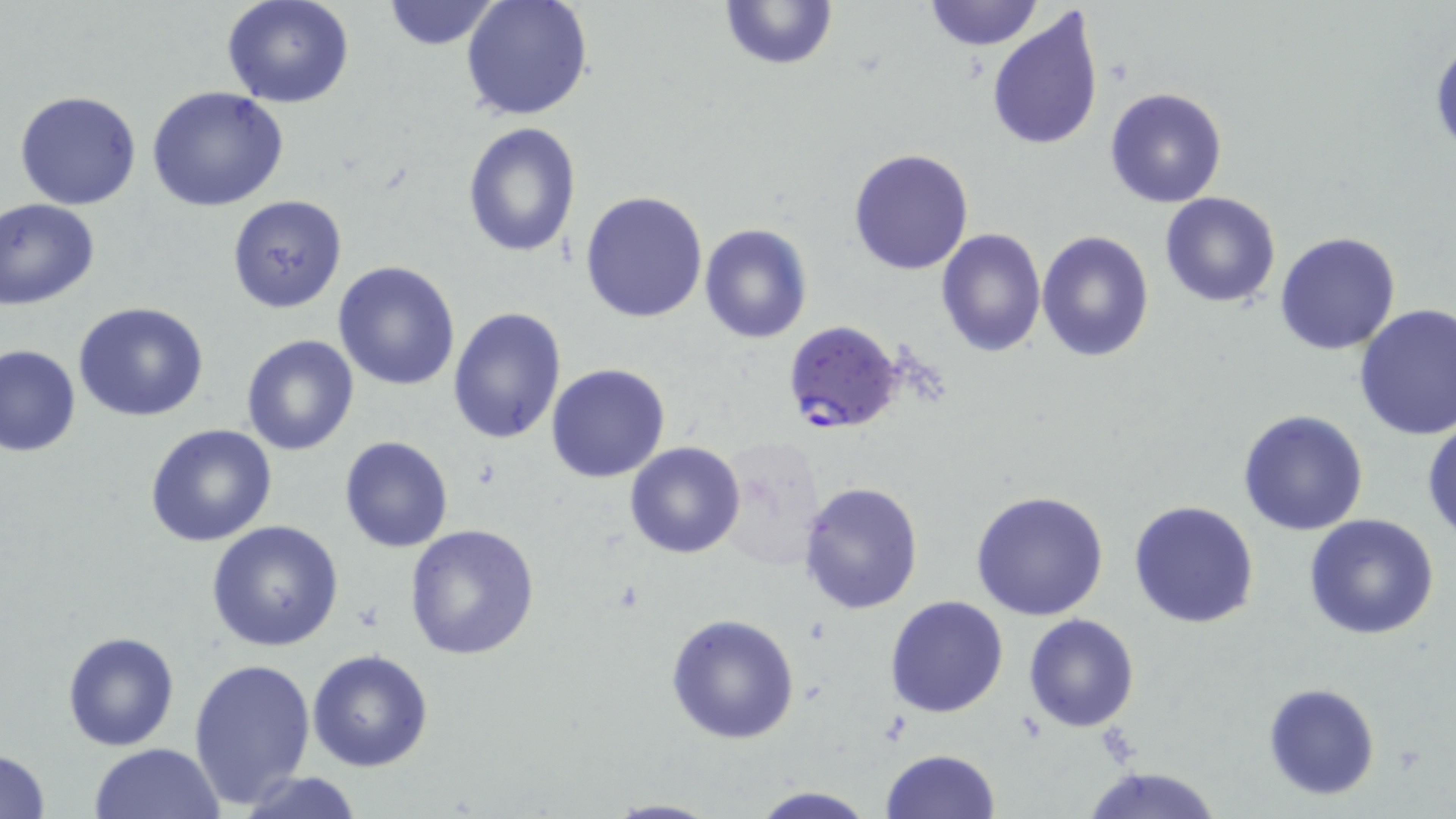
slide_level_diagnosis: Plasmodium falciparum
stain: May-Grünwald-Giemsa
modality: light microscopy
preparation: thin blood film
image_size: 1456×819 pixels
uninfected_red_blood_cell_locations: 'approximate bounding boxes as (x1,y1)-(x2,y2) corner pairs in pixels: (221,0)-(354,108), (380,0)-(502,51), (461,0)-(594,123), (717,0)-(838,71), (922,0)-(1044,49), (988,7)-(1105,151), (1429,33)-(1456,155), (147,87)-(292,213), (1104,87)-(1228,208), (14,90)-(142,209), (461,121)-(582,256), (847,148)-(974,275), (579,189)-(709,324), (1160,193)-(1283,308), (226,194)-(347,315), (1,198)-(101,309), (699,223)-(813,344), (937,228)-(1045,357), (1037,228)-(1155,362), (1274,231)-(1402,355), (332,261)-(461,391), (73,302)-(210,422), (1353,303)-(1456,440), (447,306)-(567,446), (241,336)-(359,456), (1,345)-(80,457), (546,363)-(671,483), (1237,409)-(1370,536), (1423,419)-(1456,542), (144,424)-(278,549), (339,436)-(453,553), (711,437)-(830,572), (624,441)-(746,559), (797,480)-(925,617), (970,490)-(1109,621), (1128,500)-(1261,629), (1302,515)-(1441,640), (206,520)-(346,651), (403,523)-(540,660), (884,595)-(1009,718), (665,612)-(801,744), (1024,613)-(1139,732), (62,631)-(179,750), (307,649)-(435,773), (188,657)-(315,810), (1263,682)-(1380,801), (87,742)-(224,819), (881,745)-(1000,819), (0,747)-(51,819), (1079,764)-(1224,819), (235,771)-(369,819), (746,786)-(880,819), (600,798)-(726,818)'
plasmodium_falciparum_infected_red_blood_cell_locations: 'approximate bounding boxes as (x1,y1)-(x2,y2) corner pairs in pixels: (783,321)-(906,437)'
field_of_view: single
magnification: 1000x